Assess the morphology of the erythrocytes.
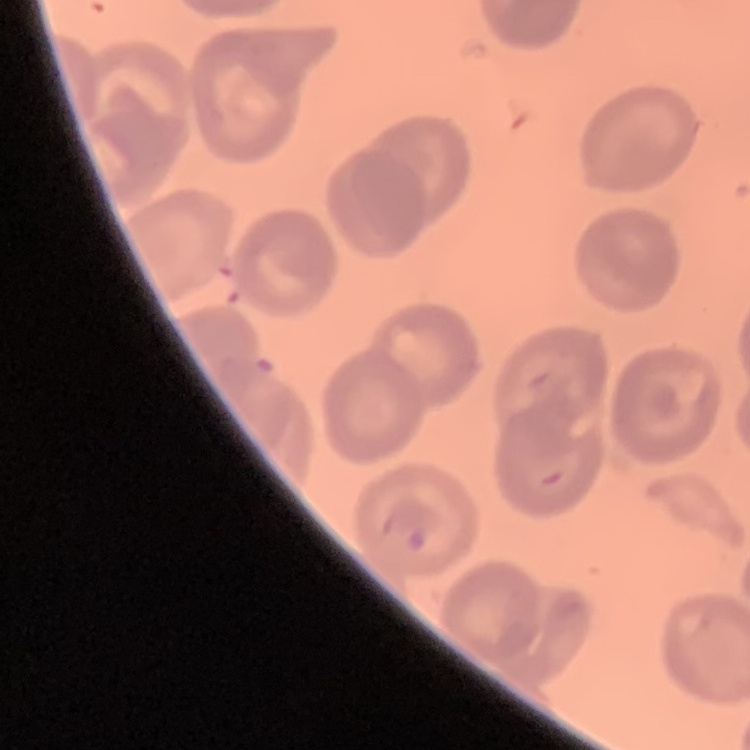
No rouleaux formation.

Summary:
  - Image type: square crop of a larger photomicrograph
  - Stain: Field's or Giemsa
  - Preparation: thin blood film